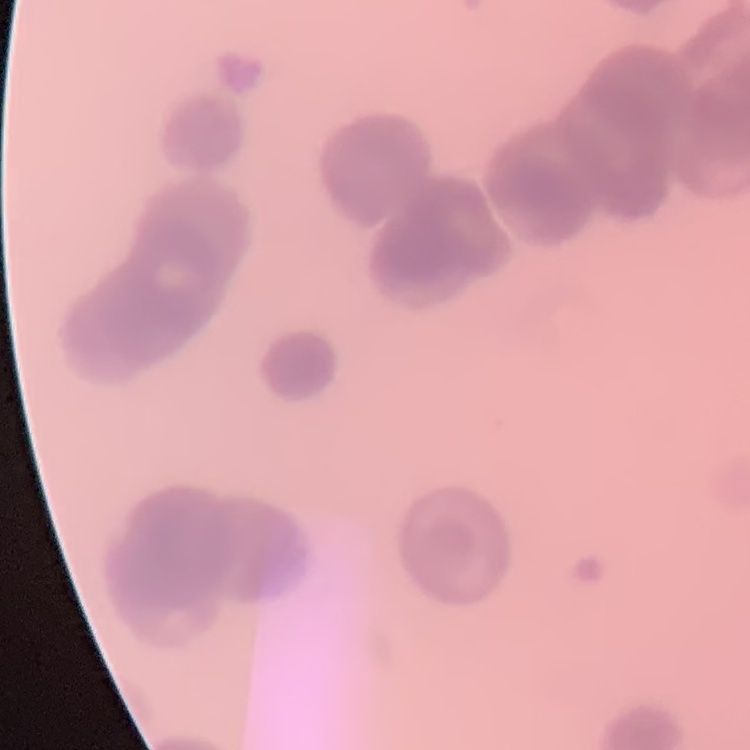

erythrocyte_morphology: rouleaux formation
image_type: one tile cut from a larger photomicrograph
preparation: thin blood smear
stain: Field's or Giemsa